Identify the blood parasite species.
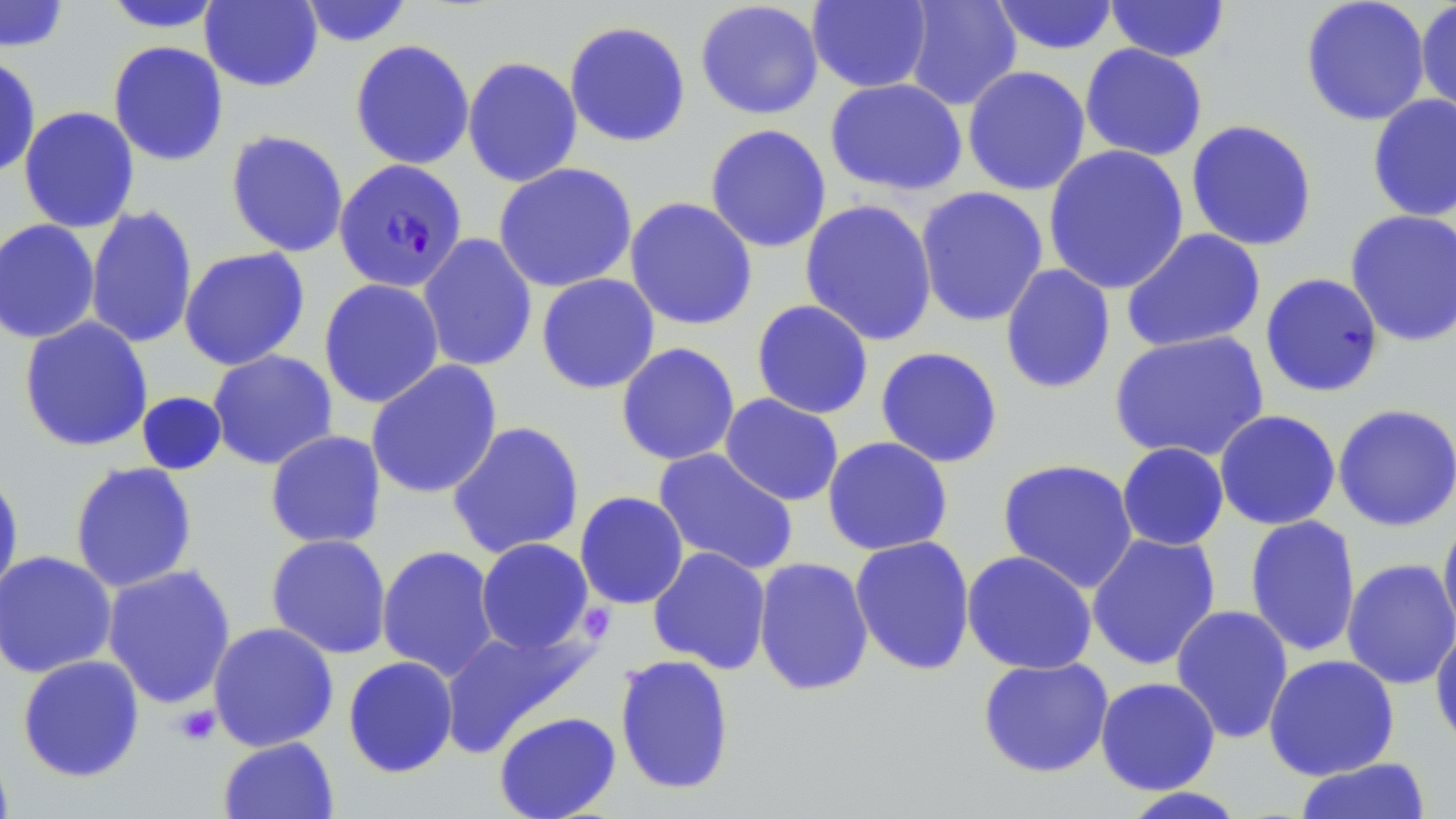

Plasmodium falciparum.

Summary:
  - Coordinate format: approximate bounding boxes as named x1/y1/x2/y2 corners in pixels
  - Platelet locations: (x1=173, y1=704, x2=221, y2=746)
  - Uninfected red blood cell locations: (x1=200, y1=0, x2=324, y2=92), (x1=298, y1=0, x2=415, y2=47), (x1=903, y1=0, x2=1022, y2=111), (x1=990, y1=0, x2=1119, y2=56), (x1=1300, y1=0, x2=1431, y2=127), (x1=0, y1=1, x2=71, y2=52), (x1=101, y1=1, x2=228, y2=33), (x1=695, y1=1, x2=824, y2=120), (x1=807, y1=1, x2=932, y2=93), (x1=1104, y1=1, x2=1231, y2=63), (x1=1415, y1=1, x2=1456, y2=124), (x1=564, y1=20, x2=691, y2=147), (x1=349, y1=39, x2=475, y2=170), (x1=107, y1=40, x2=229, y2=167), (x1=1079, y1=43, x2=1208, y2=162), (x1=0, y1=54, x2=41, y2=179), (x1=462, y1=56, x2=583, y2=188), (x1=962, y1=65, x2=1091, y2=196), (x1=824, y1=78, x2=968, y2=196), (x1=1366, y1=93, x2=1456, y2=222), (x1=18, y1=106, x2=140, y2=233), (x1=1185, y1=119, x2=1318, y2=252), (x1=704, y1=124, x2=832, y2=253), (x1=225, y1=129, x2=349, y2=258), (x1=1043, y1=144, x2=1190, y2=295), (x1=493, y1=162, x2=638, y2=293), (x1=915, y1=186, x2=1049, y2=328), (x1=625, y1=196, x2=758, y2=331), (x1=799, y1=198, x2=938, y2=347), (x1=84, y1=205, x2=198, y2=349), (x1=1344, y1=209, x2=1456, y2=347), (x1=0, y1=218, x2=101, y2=344), (x1=1121, y1=228, x2=1266, y2=353), (x1=418, y1=233, x2=538, y2=373), (x1=179, y1=247, x2=311, y2=371), (x1=1000, y1=264, x2=1115, y2=395), (x1=536, y1=273, x2=660, y2=394), (x1=1259, y1=273, x2=1385, y2=398), (x1=318, y1=278, x2=445, y2=408), (x1=751, y1=299, x2=874, y2=419), (x1=18, y1=316, x2=154, y2=453), (x1=1109, y1=330, x2=1270, y2=463), (x1=615, y1=342, x2=741, y2=466), (x1=875, y1=346, x2=1004, y2=468), (x1=207, y1=349, x2=338, y2=470), (x1=365, y1=359, x2=503, y2=500), (x1=135, y1=391, x2=227, y2=476), (x1=719, y1=393, x2=844, y2=506), (x1=1332, y1=403, x2=1456, y2=531), (x1=1214, y1=409, x2=1342, y2=530), (x1=447, y1=420, x2=585, y2=560), (x1=264, y1=430, x2=387, y2=549), (x1=822, y1=436, x2=953, y2=556), (x1=1117, y1=442, x2=1229, y2=551), (x1=652, y1=448, x2=798, y2=576), (x1=997, y1=458, x2=1139, y2=593), (x1=69, y1=461, x2=198, y2=593), (x1=0, y1=466, x2=25, y2=605), (x1=574, y1=491, x2=689, y2=609), (x1=1437, y1=512, x2=1456, y2=645), (x1=1244, y1=515, x2=1362, y2=657), (x1=1086, y1=531, x2=1222, y2=671), (x1=265, y1=533, x2=392, y2=659), (x1=849, y1=535, x2=976, y2=676), (x1=475, y1=538, x2=594, y2=655), (x1=376, y1=545, x2=501, y2=682), (x1=647, y1=546, x2=772, y2=674), (x1=961, y1=549, x2=1098, y2=675), (x1=0, y1=550, x2=117, y2=679), (x1=753, y1=557, x2=874, y2=696), (x1=1341, y1=557, x2=1456, y2=690), (x1=101, y1=564, x2=237, y2=709), (x1=1170, y1=604, x2=1294, y2=744), (x1=207, y1=622, x2=339, y2=751), (x1=1430, y1=624, x2=1456, y2=752), (x1=439, y1=626, x2=593, y2=756), (x1=614, y1=653, x2=736, y2=795), (x1=1263, y1=653, x2=1400, y2=780), (x1=17, y1=654, x2=146, y2=783), (x1=342, y1=656, x2=459, y2=778), (x1=976, y1=657, x2=1114, y2=778), (x1=1094, y1=676, x2=1221, y2=795), (x1=493, y1=711, x2=622, y2=819), (x1=217, y1=736, x2=339, y2=819), (x1=0, y1=739, x2=15, y2=818), (x1=1293, y1=757, x2=1432, y2=818), (x1=1117, y1=786, x2=1250, y2=818)
  - Plasmodium falciparum-infected red blood cell locations: (x1=334, y1=158, x2=467, y2=292)
  - Preparation: thin blood film
  - Stain: May-Grünwald-Giemsa
  - Field of view: one of a larger specimen
  - Magnification: 1000x
  - Image size: 1456×819 pixels
  - Modality: optical microscopy